Classify this cell by malaria status.
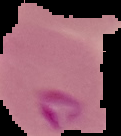

Parasitized.

Summary:
  - Preparation: thin blood smear
  - Image type: cell region segmented out of the field of view; surrounding area masked to black
  - Image size: 121×136 pixels